Find the red blood cells that are infected with P. falciparum, and any of indeterminate infection status.
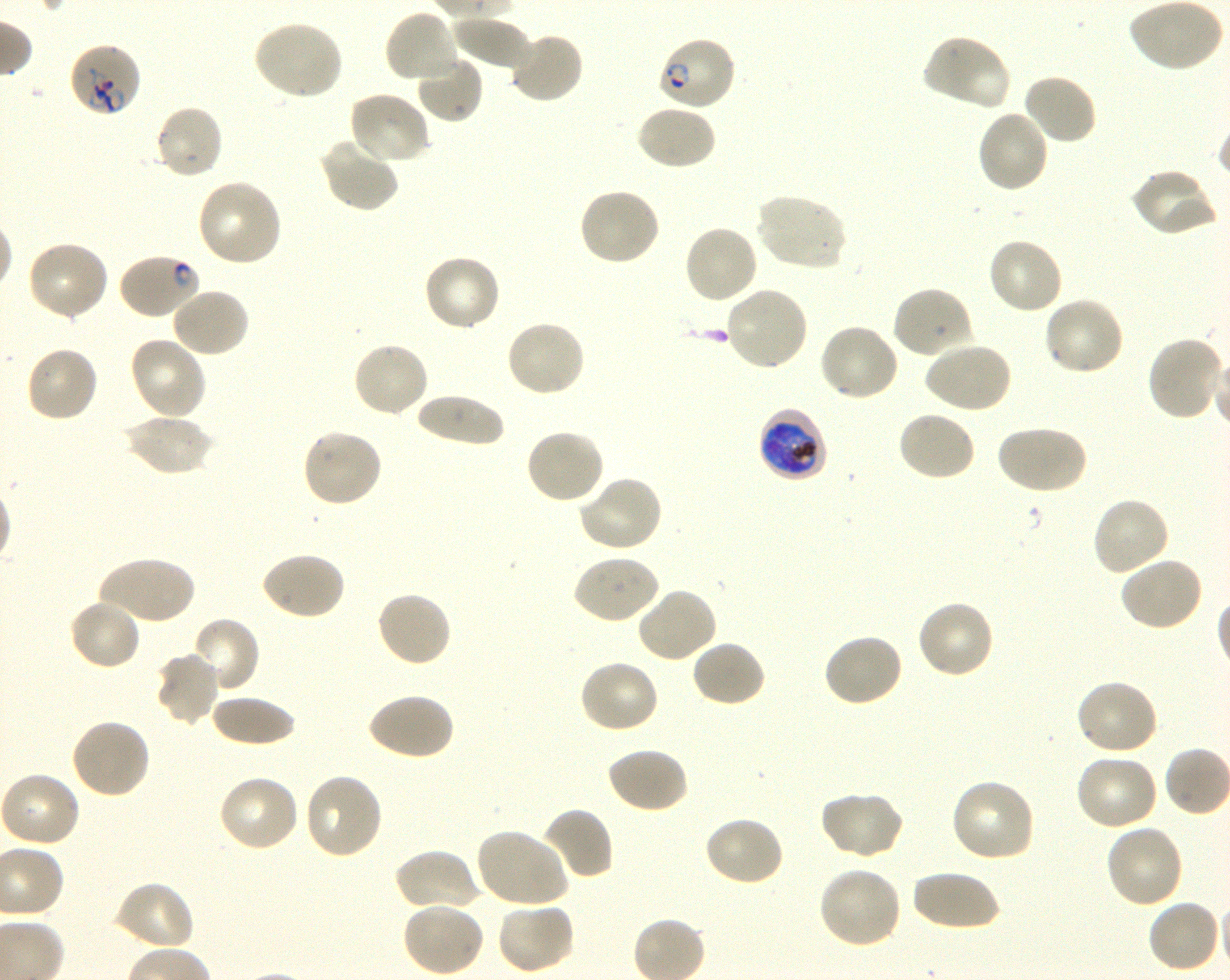
Approximate bounding boxes as (x1, y1, x2, y2) in pixels. Not every red blood cell is marked. A life-cycle stage — or a range of stages, where the recorded stages span more than one — follows each staged infected red blood cell.
Infected red blood cells: (657, 34, 737, 112) ring; (758, 407, 828, 484) late trophozoite to early schizont.
Red blood cells of indeterminate infection status: (70, 44, 144, 117), (118, 252, 201, 321).

locations of uninfected red blood cells = (1129, 1, 1225, 74), (383, 7, 461, 84), (451, 16, 532, 72), (250, 20, 344, 101), (508, 30, 584, 105), (920, 33, 1010, 111), (414, 53, 484, 124), (1022, 72, 1098, 146), (347, 90, 432, 165), (152, 104, 225, 181), (636, 105, 717, 171), (975, 109, 1051, 194), (320, 137, 399, 214), (1130, 166, 1220, 237), (196, 178, 283, 268), (578, 186, 661, 267), (754, 192, 848, 271), (681, 224, 759, 305), (986, 237, 1064, 316), (26, 239, 110, 322), (422, 253, 503, 333), (724, 284, 810, 372), (892, 285, 974, 359), (170, 286, 251, 358), (1042, 296, 1125, 377), (505, 318, 587, 397), (817, 322, 899, 403), (129, 335, 209, 420), (1146, 335, 1225, 421), (351, 340, 430, 418), (922, 340, 1013, 414), (25, 346, 100, 423), (413, 393, 505, 447), (897, 410, 977, 482), (122, 412, 214, 477), (994, 424, 1087, 496), (301, 427, 383, 509), (523, 427, 606, 505), (577, 474, 664, 553), (1091, 494, 1171, 576), (259, 551, 346, 621), (571, 554, 660, 625), (98, 555, 195, 626), (1119, 555, 1205, 631), (636, 586, 718, 664), (375, 591, 454, 669), (68, 597, 142, 671), (916, 599, 995, 680), (186, 616, 261, 696), (821, 633, 905, 708), (691, 639, 767, 708), (154, 651, 221, 726), (578, 659, 660, 735), (1074, 679, 1160, 757), (366, 692, 455, 762), (208, 695, 298, 748), (70, 718, 152, 799), (606, 746, 689, 814), (1074, 753, 1160, 831), (0, 771, 82, 847), (302, 773, 385, 861), (217, 775, 301, 853), (950, 777, 1037, 863), (817, 790, 905, 861), (541, 806, 614, 882), (703, 815, 786, 887), (1104, 823, 1184, 908), (475, 827, 569, 908), (394, 848, 479, 913), (817, 866, 903, 949), (911, 869, 999, 932), (113, 879, 196, 952), (1146, 898, 1222, 974), (494, 900, 576, 975), (401, 902, 485, 977)
field of view = one from this slide
stain = Giemsa
culture = P. falciparum strain 3D7, shaking, in vitro
donor blood group = O+
preparation = thin blood film
objective = 100x, oil immersion, numerical aperture 1.30
image size = 1230×980 pixels